Classify this cell by malaria status.
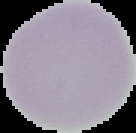

Uninfected.

image size = 136×133 pixels
image type = segmented cell region with the area outside set to black
preparation = thin blood smear